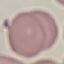
Summary:
  - Result: negative for malaria parasites
  - Capture: smartphone through the microscope eyepiece
  - Stain: Giemsa
  - Image type: automatically extracted cell patch, resized to 64 × 64 pixels
  - Preparation: thin blood smear